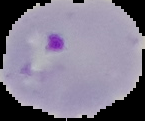
image size = 145×121 pixels
preparation = thin blood smear
image type = segmented cell region with the area outside set to black
result = Plasmodium parasites identified